Describe the morphology of the erythrocytes.
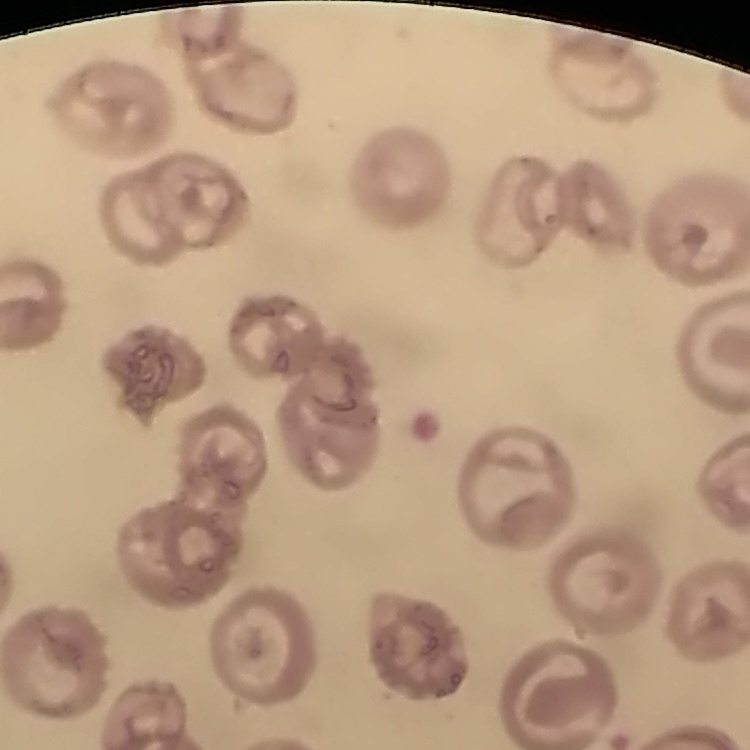
No rouleaux formation.

Thin peripheral smear. Stained with either Field's or Giemsa. Square crop of a larger photomicrograph.